Assess the morphology of the erythrocytes.
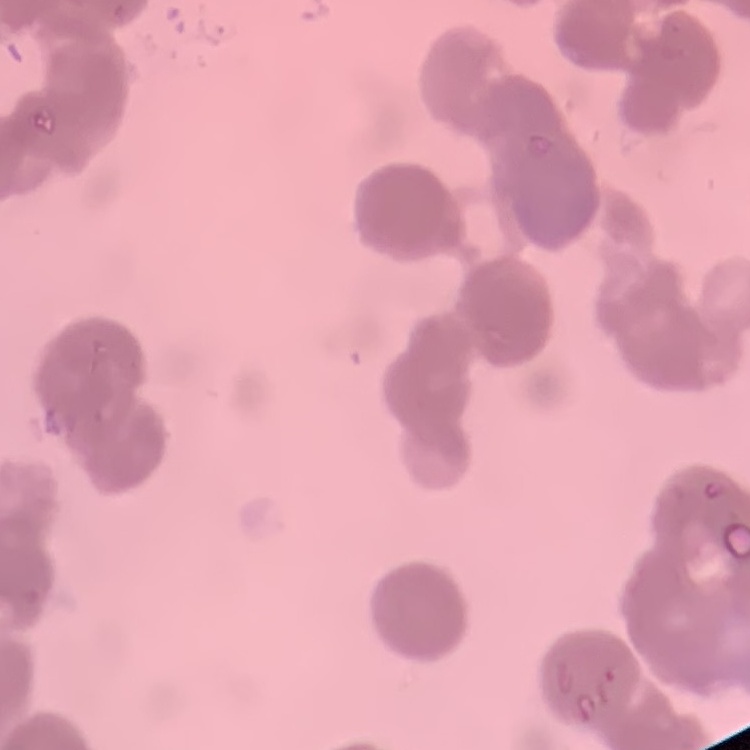

They show rouleaux formation.

Thin blood film. Square crop of a larger photomicrograph. Field's or Giemsa stain.